Assess this cell for malaria.
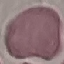
Uninfected.

image_type: cell patch, automatically extracted from a larger field of view and resized to 64 × 64 pixels
capture: smartphone camera at the microscope eyepiece
stain: Giemsa
preparation: thin blood film